Name the blood parasite species.
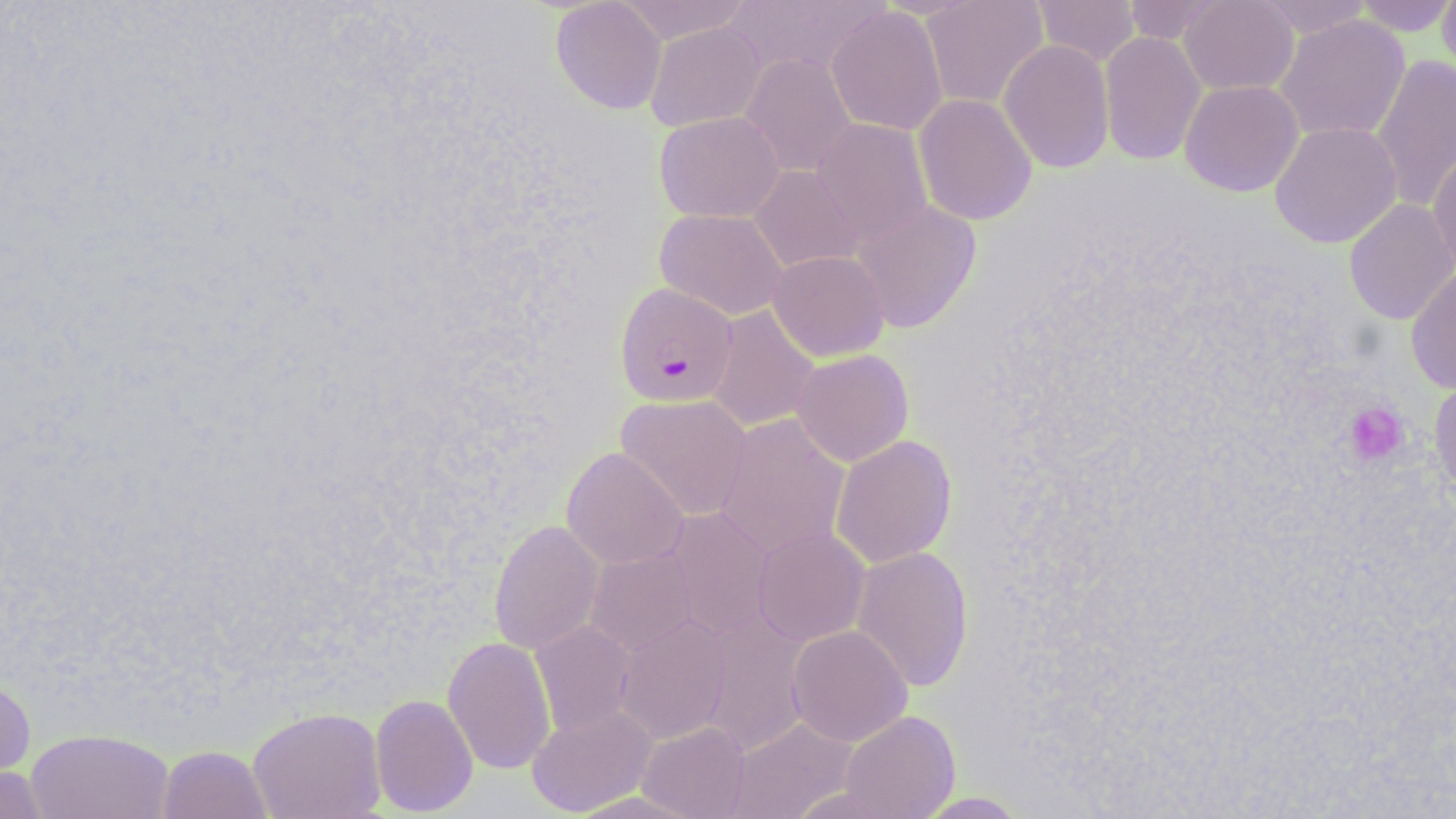

Plasmodium falciparum.

magnification = 1000x
platelet locations = approximate bounding boxes as [x1, y1, x2, y2] in pixels: [1344, 401, 1410, 467]
stain = May-Grünwald-Giemsa
image size = 1456×819 pixels
modality = light microscopy
preparation = thin blood smear
Plasmodium falciparum-infected red blood cell locations = approximate bounding boxes as [x1, y1, x2, y2] in pixels: [614, 282, 738, 407]
uninfected red blood cell locations = approximate bounding boxes as [x1, y1, x2, y2] in pixels: [550, 0, 667, 115], [615, 0, 751, 44], [921, 0, 1048, 110], [1031, 0, 1141, 66], [1122, 0, 1226, 45], [1179, 0, 1299, 95], [1255, 0, 1374, 38], [1352, 0, 1456, 36], [1437, 0, 1456, 84], [720, 1, 886, 78], [826, 6, 948, 136], [1273, 15, 1410, 143], [645, 21, 765, 131], [1099, 31, 1206, 167], [998, 40, 1115, 173], [740, 53, 856, 177], [1371, 54, 1456, 212], [1179, 80, 1304, 197], [913, 93, 1037, 225], [654, 111, 784, 223], [811, 118, 933, 246], [1269, 120, 1402, 249], [1428, 146, 1456, 279], [749, 165, 862, 273], [1343, 198, 1456, 325], [851, 200, 982, 334], [654, 208, 787, 321], [768, 250, 889, 361], [1406, 267, 1456, 394], [705, 305, 820, 432], [792, 349, 913, 466], [1429, 377, 1456, 499], [616, 394, 752, 521], [714, 413, 851, 560], [831, 434, 957, 568], [561, 447, 689, 569], [661, 506, 776, 641], [488, 519, 603, 655], [752, 527, 870, 646], [851, 545, 974, 693], [585, 548, 699, 657], [696, 611, 811, 756], [615, 614, 732, 744], [530, 621, 636, 736], [787, 625, 912, 746], [442, 636, 556, 775], [0, 671, 36, 790], [370, 694, 478, 816], [526, 705, 657, 817], [248, 706, 386, 819], [839, 710, 960, 819], [727, 717, 857, 819], [637, 722, 751, 818], [26, 729, 174, 819], [158, 745, 272, 819], [0, 763, 49, 819], [912, 791, 1031, 818]
field of view = one of a larger specimen